Assess this cell for malaria.
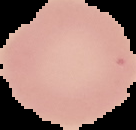

Uninfected.

The area outside the segmented cell region is set to black. Image is 136×130 pixels. From a thin blood smear.